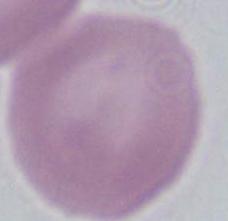
Summary:
  - Identification: erythrocyte
  - Modality: photomicrograph
  - Magnification: 1000x